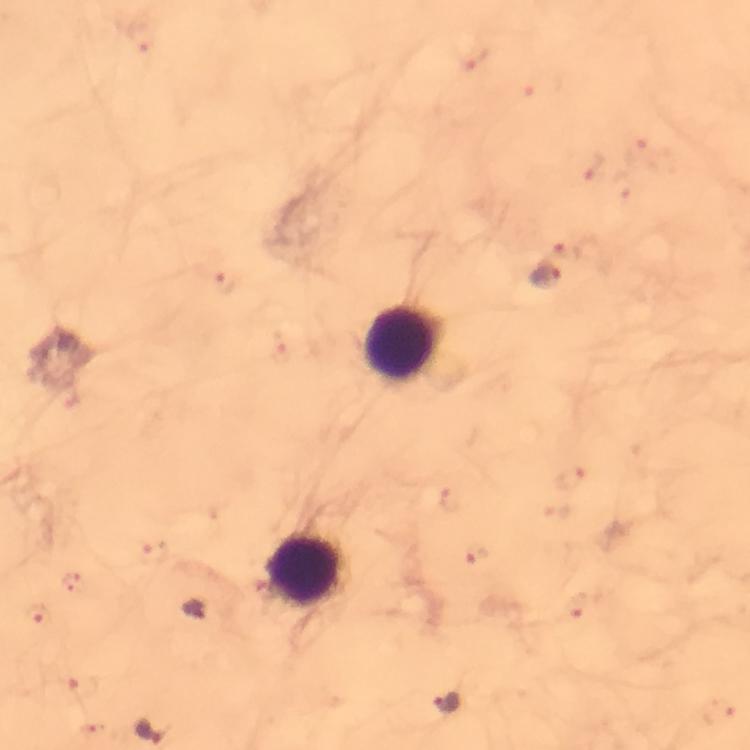
Approximate object centers, in pixels from the top-left corner. Plasmodium parasite locations: (x=592, y=165), (x=544, y=274), (x=225, y=282), (x=571, y=476), (x=451, y=500), (x=476, y=554), (x=153, y=555), (x=578, y=606), (x=35, y=614), (x=196, y=614), (x=84, y=688), (x=446, y=703), (x=719, y=711), (x=152, y=731). Leukocyte locations: (x=402, y=344), (x=303, y=570). Immersion oil was used. Thick blood smear. Giemsa-stained preparation. Image is 750×750 pixels. Photographed with a smartphone mounted on the microscope. At 100x magnification. Cropped region of a single field of view. From a malaria diagnostic workup.